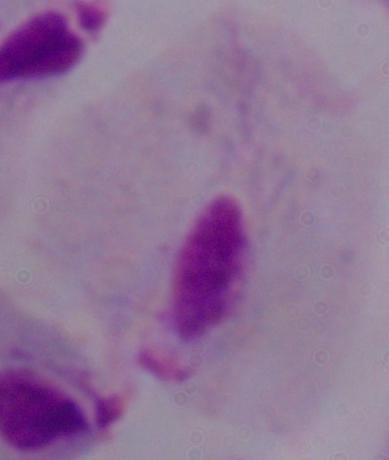

identification = trichomonad
magnification = 1000x
modality = photomicrograph